Outline each blood parasite and name the species.
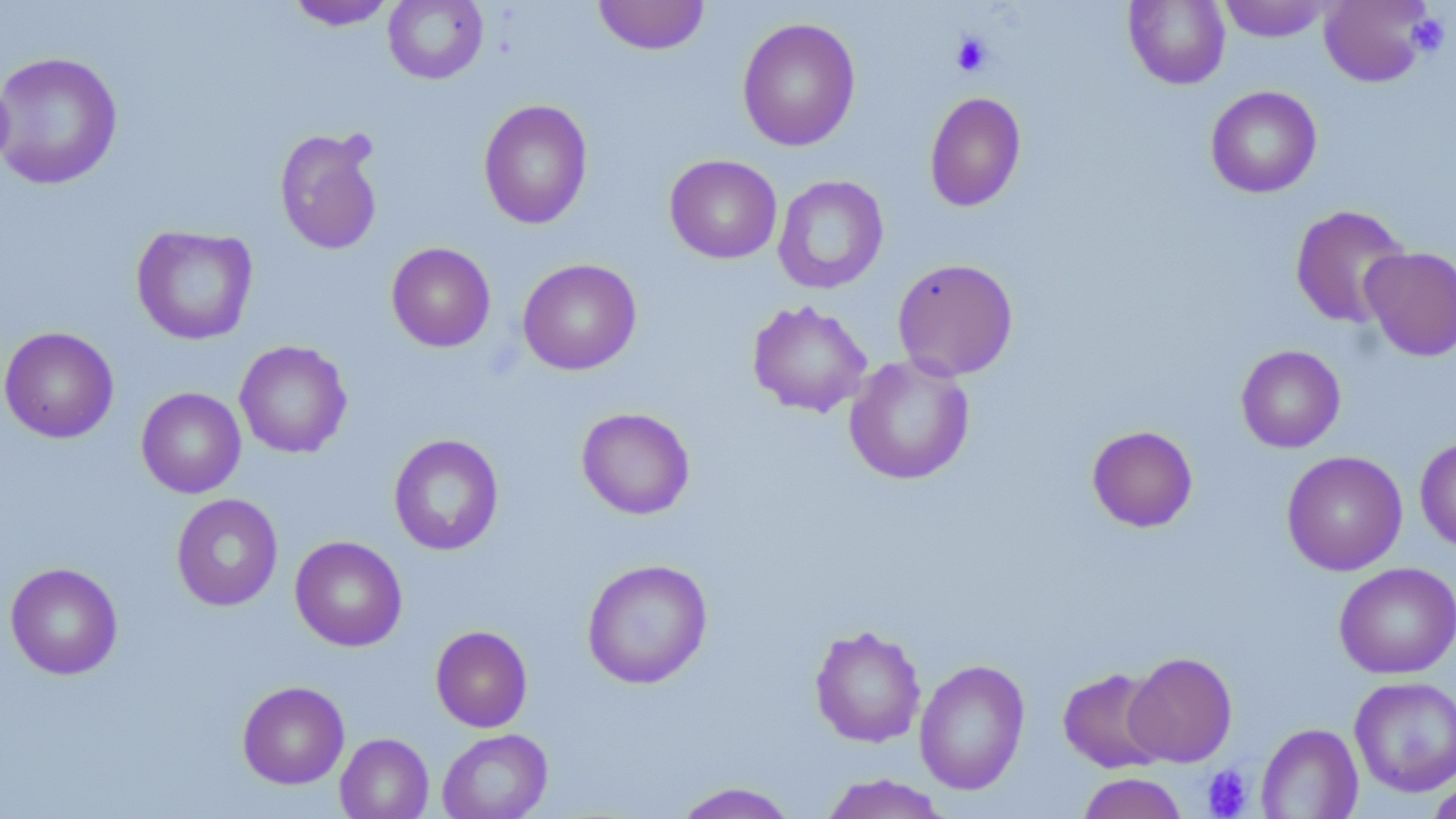

No blood parasites seen.

Approximate bounding boxes as (x1,y1)-(x2,y2) corner pairs in pixels. Platelet locations: (1407,14)-(1451,56), (951,32)-(993,77), (1201,765)-(1253,818). Uninfected red blood cell locations: (383,0)-(488,84), (593,0)-(710,55), (1123,0)-(1230,89), (1218,0)-(1332,42), (1319,0)-(1434,87), (285,1)-(398,31), (737,17)-(860,152), (0,50)-(123,190), (1206,86)-(1322,198), (924,91)-(1027,212), (478,99)-(593,230), (274,127)-(384,256), (664,155)-(782,264), (773,175)-(889,294), (1289,205)-(1412,329), (131,225)-(258,345), (386,242)-(495,352), (1360,246)-(1456,361), (517,258)-(641,375), (892,258)-(1019,381), (747,300)-(872,417), (0,326)-(119,443), (234,340)-(352,459), (1236,345)-(1345,453), (844,354)-(975,485), (136,387)-(246,498), (576,407)-(695,519), (1086,425)-(1199,532), (388,433)-(504,555), (1415,436)-(1456,553), (1281,450)-(1408,576), (171,493)-(283,611), (290,535)-(407,651), (582,558)-(713,689), (5,562)-(123,680), (1334,562)-(1456,678), (809,624)-(926,748), (430,625)-(532,732), (1124,652)-(1238,767), (914,659)-(1030,794), (1057,667)-(1171,773), (1349,676)-(1456,796), (237,681)-(350,789), (1256,723)-(1363,818), (437,729)-(553,819), (335,733)-(434,819), (1076,772)-(1189,819), (818,774)-(952,819), (1426,775)-(1456,819), (671,781)-(801,818). Slide-level diagnosis: negative for blood parasites. Single field of view. Light microscopy. Thin blood smear. Captured at 1000x magnification. May-Grünwald-Giemsa stain. Image is 1456×819 pixels.